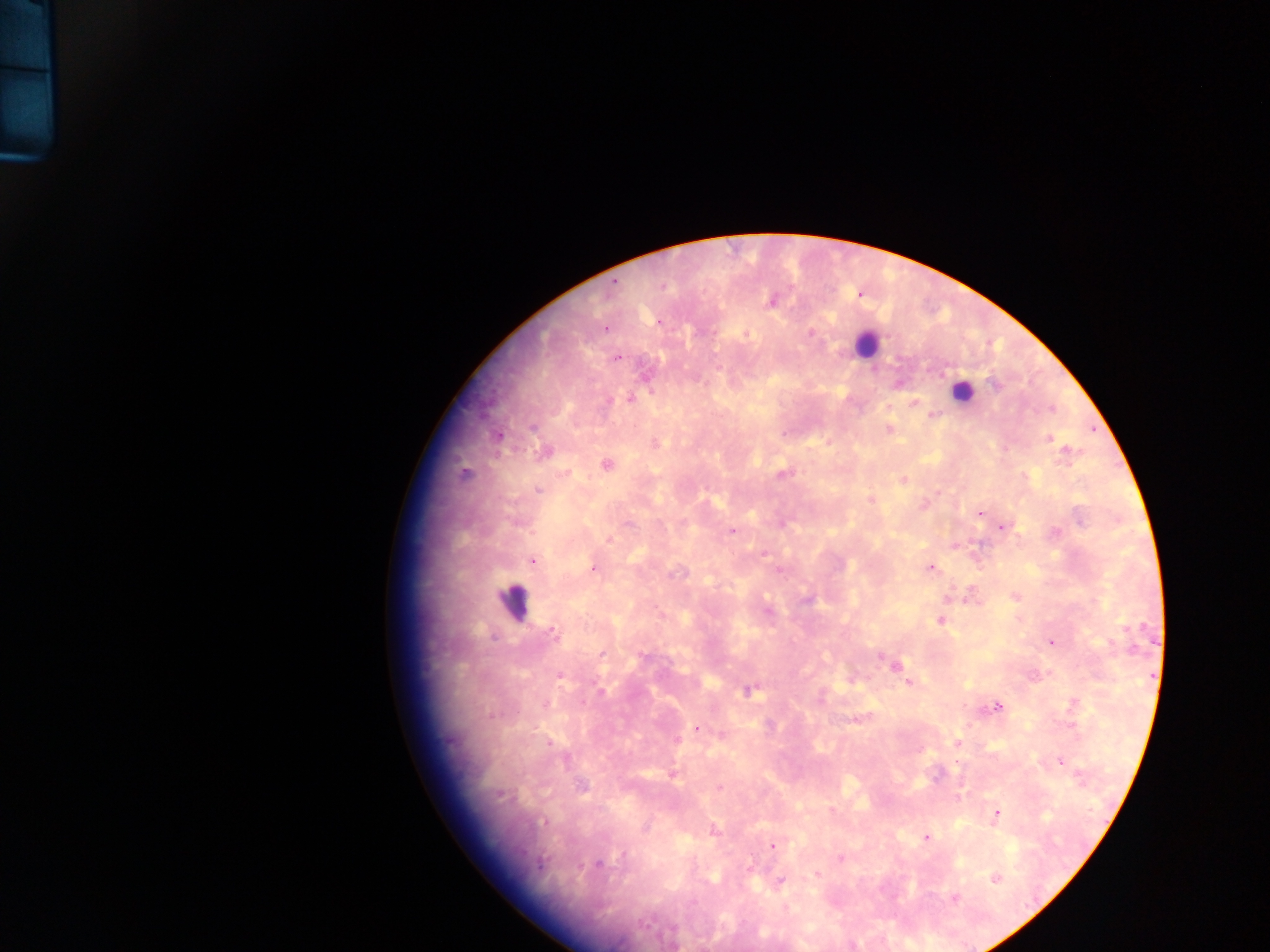
Approximate centers as (x, y) in pixels.
Summary:
  - Leukocyte locations: (867, 344), (962, 391), (513, 600)
  - Malaria parasite locations: (614, 283), (859, 294), (772, 300), (605, 328), (810, 332), (617, 358), (899, 384), (995, 385), (631, 398), (606, 400), (913, 403), (1050, 408), (932, 415), (533, 426), (889, 430), (497, 435), (1048, 438), (654, 442), (544, 452), (605, 464), (783, 473), (464, 474), (902, 480), (538, 489), (870, 500), (981, 512), (1002, 526), (731, 530), (608, 539), (532, 560), (593, 568), (930, 568), (1015, 596), (948, 598), (661, 615), (941, 620), (552, 631), (1051, 642), (601, 655), (894, 665), (560, 675), (909, 682), (749, 690), (995, 706), (857, 719), (697, 728), (722, 734), (675, 740), (957, 742), (1059, 761), (671, 772), (581, 786), (717, 788), (996, 813), (713, 831), (925, 837), (772, 845), (840, 858), (597, 864), (817, 874), (995, 878), (780, 880), (953, 897)
  - Preparation: thick blood smear
  - Country: Ghana
  - Capture: mobile-phone photograph through a microscope
  - Field of view: single
  - Image size: 1270×952 pixels